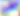

Toxoplasma gondii is shown. 400x magnification. Micrograph.